Classify this cell by malaria status.
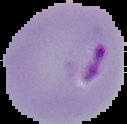
It is parasitized.

{
  "image_size": "127×124 pixels",
  "preparation": "thin blood film",
  "image_type": "segmented cell region on a black background"
}